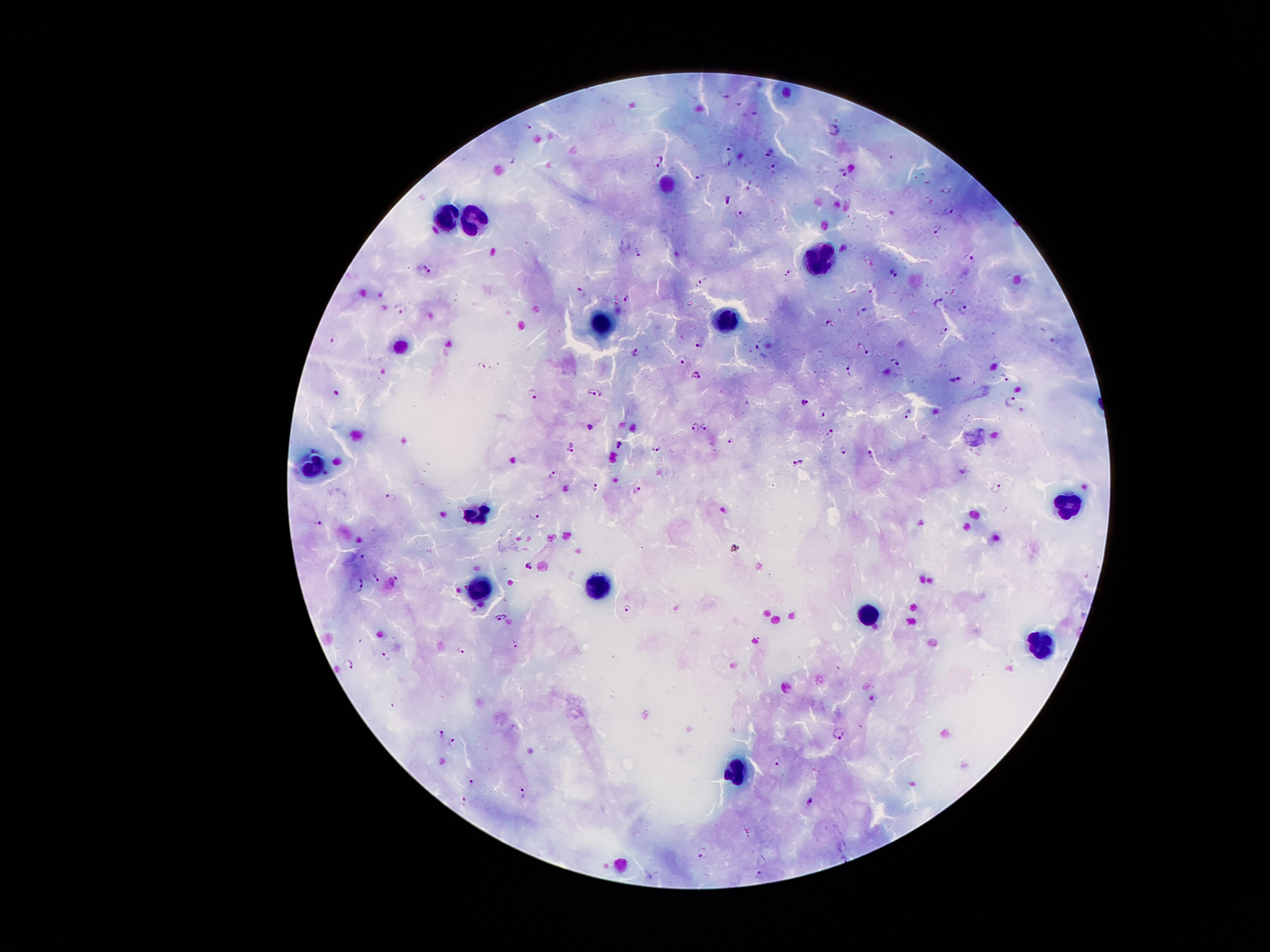

{
  "stain": "Giemsa",
  "leukocyte_locations": "approximate object centers, in pixels from the top-left corner: (x=666, y=182), (x=440, y=212), (x=469, y=212), (x=823, y=255), (x=727, y=317), (x=602, y=322), (x=306, y=472), (x=1066, y=509), (x=475, y=514), (x=483, y=589), (x=598, y=589), (x=870, y=617), (x=1039, y=646), (x=732, y=768)",
  "preparation": "thick peripheral-blood smear",
  "malaria_parasite_locations": "approximate object centers, in pixels from the top-left corner: (x=528, y=127), (x=835, y=129), (x=732, y=146), (x=771, y=152), (x=657, y=161), (x=731, y=163), (x=774, y=167), (x=843, y=171), (x=700, y=175), (x=727, y=201), (x=950, y=209), (x=738, y=213), (x=937, y=231), (x=638, y=250), (x=970, y=261), (x=422, y=269), (x=896, y=272), (x=789, y=273), (x=705, y=281), (x=581, y=293), (x=628, y=297), (x=939, y=299), (x=964, y=309), (x=400, y=310), (x=943, y=332), (x=334, y=341), (x=700, y=342), (x=864, y=348), (x=638, y=350), (x=684, y=358), (x=895, y=362), (x=850, y=370), (x=696, y=373), (x=1005, y=375), (x=955, y=377), (x=597, y=392), (x=532, y=394), (x=803, y=400), (x=1013, y=402), (x=908, y=412), (x=825, y=413), (x=695, y=426), (x=705, y=426), (x=590, y=427), (x=831, y=434), (x=730, y=440), (x=619, y=445), (x=571, y=447), (x=656, y=447), (x=844, y=451), (x=872, y=456), (x=798, y=460), (x=552, y=475), (x=596, y=487), (x=995, y=489), (x=636, y=491), (x=390, y=498), (x=535, y=515), (x=320, y=522), (x=367, y=556), (x=530, y=565), (x=376, y=577), (x=394, y=582), (x=359, y=583), (x=630, y=609), (x=501, y=617), (x=515, y=645), (x=464, y=648), (x=386, y=653), (x=348, y=660), (x=443, y=731), (x=839, y=733), (x=451, y=738), (x=778, y=762), (x=474, y=781), (x=522, y=792), (x=464, y=799), (x=810, y=800), (x=703, y=852), (x=760, y=875)",
  "magnification": "100x",
  "field_of_view": "one from this slide",
  "capture": "smartphone through the microscope eyepiece",
  "image_size": "1270×952 pixels",
  "patient_malaria_status": "infected with Plasmodium falciparum"
}